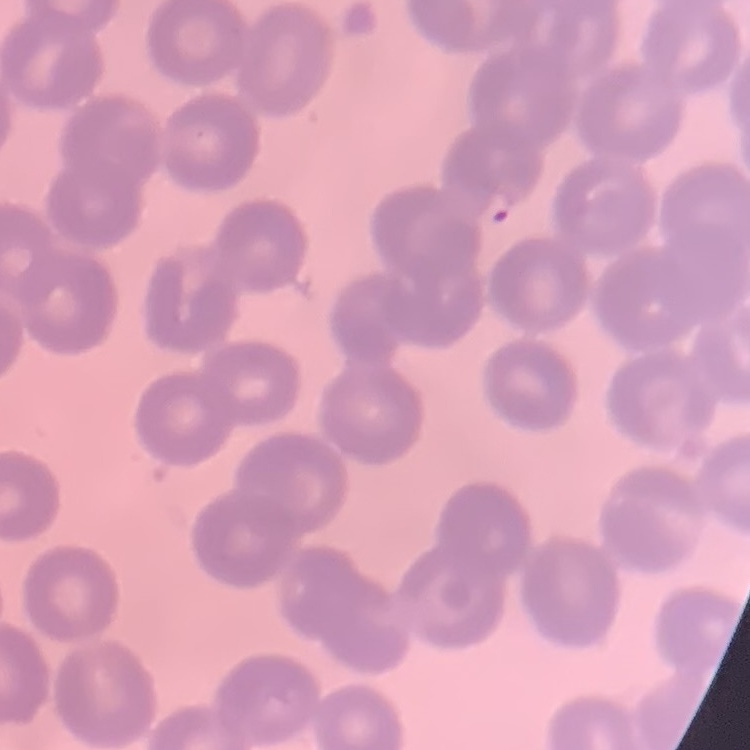
Summary:
  - Erythrocyte morphology: no rouleaux formation
  - Image type: square crop of a larger photomicrograph
  - Stain: Field's or Giemsa
  - Preparation: thin blood film